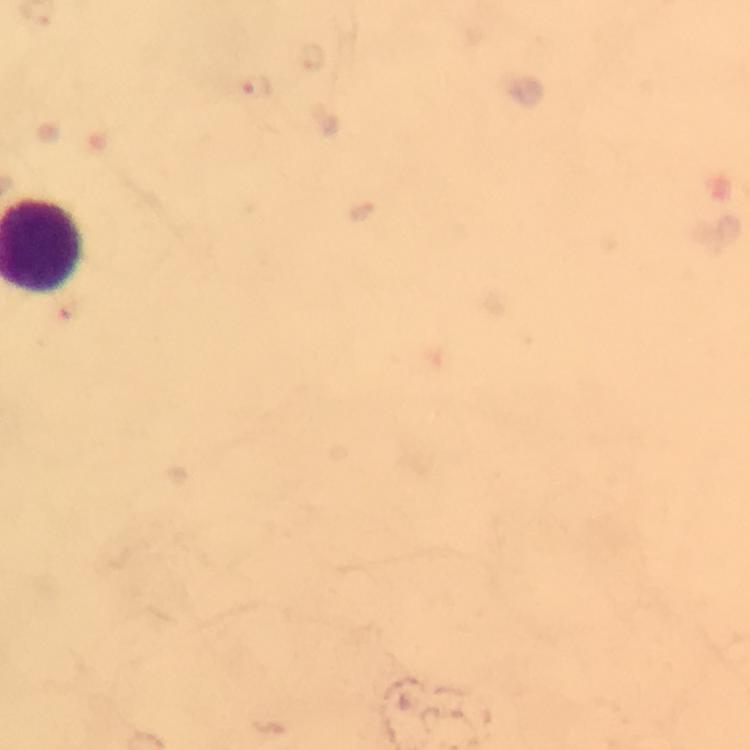

capture: smartphone photograph through a microscope
preparation: thick blood film
image_size: 750×750 pixels
malaria_parasite_locations: 'approximate centers as [x, y] in pixels: [257, 86]'
magnification: 100x
stain: Giemsa
context: from a diagnostic examination for malaria
immersion_oil: used
cropped_from: one field of view